Assess this cell for malaria.
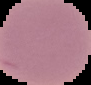
It is uninfected.

The area outside the segmented cell region is set to black. Image is 91×85 pixels. From a thin blood smear.